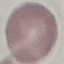
malaria_status: uninfected
capture: smartphone camera at the microscope eyepiece
preparation: thin blood smear
stain: Giemsa
image_type: cell patch, automatically extracted from a larger field of view and resized to 64 × 64 pixels